Assess the morphology of the erythrocytes.
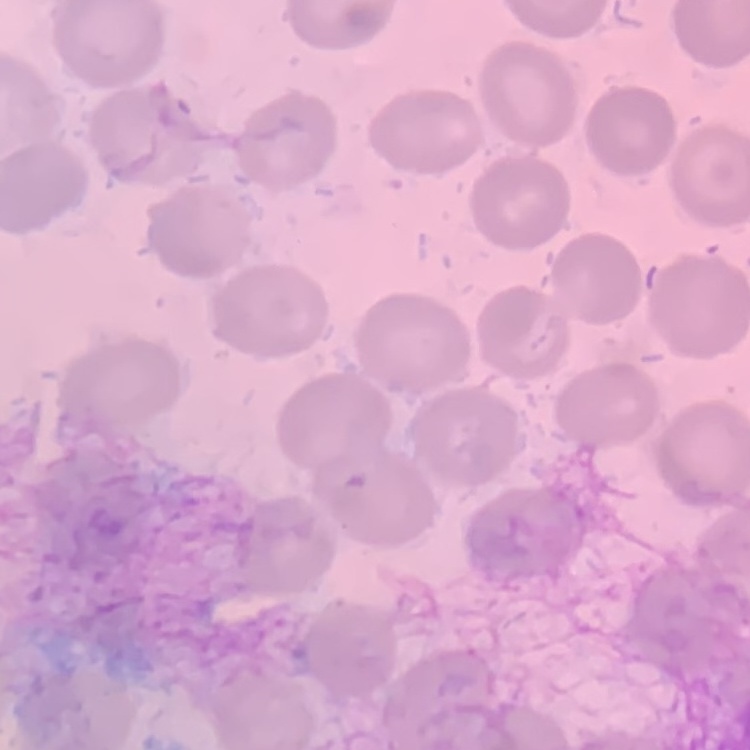
They show no rouleaux formation.

Thin blood film. Stained with either Field's or Giemsa. Square crop of a larger photomicrograph.